Point out each Plasmodium parasite.
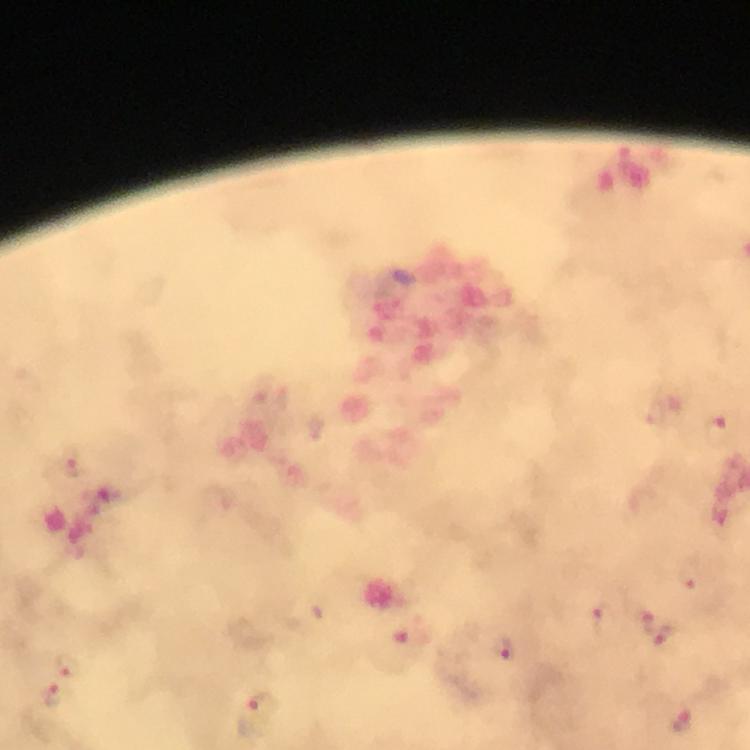
Approximate centers as {x, y} in pixels.
Plasmodium parasites: {717, 430}, {647, 622}, {662, 633}, {52, 693}, {262, 705}.

Summary:
  - Context: from a diagnostic examination for malaria
  - Preparation: thick blood film
  - Stain: Giemsa
  - Immersion oil: applied
  - Cropped from: a single field of view
  - Capture: smartphone mounted on the microscope
  - Magnification: 100x
  - Image size: 750×750 pixels